Name the blood parasite species.
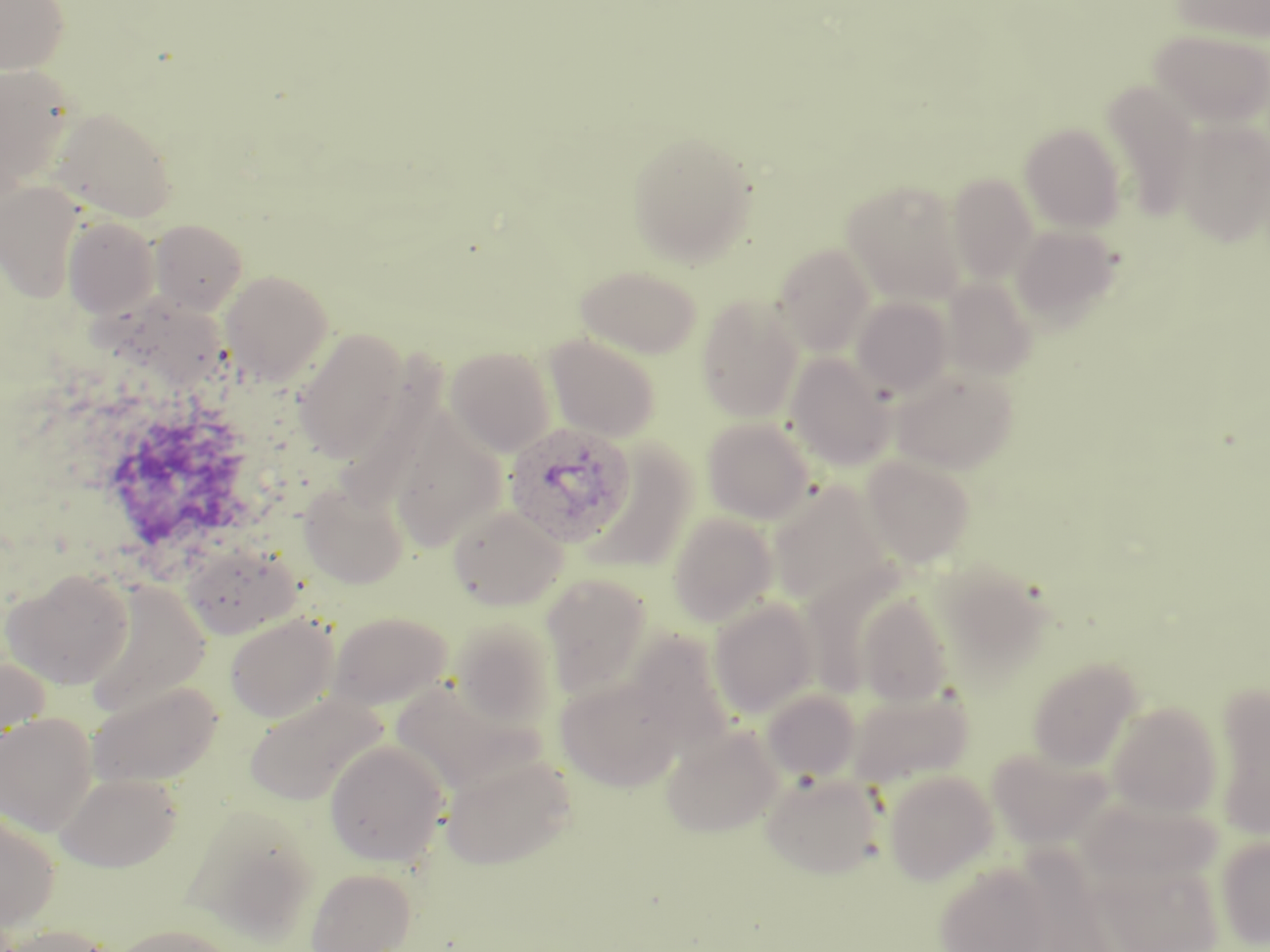

Plasmodium ovale.

Summary:
  - Coordinate format: approximate bounding boxes as named x1/y1/x2/y2 corners in pixels
  - Plasmodium ovale-infected red blood cell locations: (x1=503, y1=421, x2=636, y2=549)
  - Uninfected red blood cell locations: (x1=0, y1=0, x2=69, y2=74), (x1=1171, y1=0, x2=1270, y2=42), (x1=1150, y1=28, x2=1270, y2=128), (x1=1, y1=64, x2=77, y2=192), (x1=1101, y1=81, x2=1200, y2=219), (x1=50, y1=107, x2=178, y2=223), (x1=1174, y1=119, x2=1270, y2=247), (x1=1020, y1=123, x2=1126, y2=232), (x1=627, y1=129, x2=757, y2=267), (x1=947, y1=173, x2=1038, y2=283), (x1=842, y1=179, x2=967, y2=304), (x1=0, y1=181, x2=84, y2=302), (x1=63, y1=216, x2=160, y2=318), (x1=151, y1=219, x2=248, y2=315), (x1=1010, y1=224, x2=1123, y2=326), (x1=773, y1=244, x2=876, y2=354), (x1=576, y1=265, x2=702, y2=359), (x1=221, y1=269, x2=333, y2=384), (x1=943, y1=276, x2=1037, y2=379), (x1=91, y1=293, x2=239, y2=385), (x1=696, y1=295, x2=803, y2=422), (x1=852, y1=296, x2=953, y2=397), (x1=294, y1=329, x2=407, y2=462), (x1=545, y1=333, x2=662, y2=442), (x1=446, y1=346, x2=556, y2=456), (x1=785, y1=353, x2=896, y2=471), (x1=890, y1=369, x2=1019, y2=473), (x1=388, y1=408, x2=506, y2=553), (x1=702, y1=417, x2=815, y2=523), (x1=582, y1=442, x2=699, y2=573), (x1=861, y1=455, x2=976, y2=567), (x1=767, y1=479, x2=895, y2=611), (x1=300, y1=482, x2=408, y2=589), (x1=448, y1=504, x2=568, y2=610), (x1=668, y1=512, x2=778, y2=628), (x1=182, y1=545, x2=300, y2=639), (x1=2, y1=568, x2=135, y2=689), (x1=540, y1=573, x2=653, y2=700), (x1=83, y1=578, x2=212, y2=716), (x1=855, y1=593, x2=953, y2=706), (x1=708, y1=598, x2=818, y2=719), (x1=328, y1=611, x2=452, y2=710), (x1=225, y1=613, x2=339, y2=723), (x1=450, y1=617, x2=559, y2=727), (x1=626, y1=629, x2=739, y2=757), (x1=0, y1=653, x2=50, y2=758), (x1=1028, y1=656, x2=1143, y2=771), (x1=555, y1=676, x2=683, y2=790), (x1=85, y1=680, x2=223, y2=789), (x1=1211, y1=683, x2=1270, y2=839), (x1=845, y1=686, x2=973, y2=788), (x1=761, y1=689, x2=861, y2=782), (x1=244, y1=692, x2=387, y2=805), (x1=1106, y1=701, x2=1223, y2=818), (x1=0, y1=712, x2=98, y2=835), (x1=661, y1=723, x2=785, y2=838), (x1=324, y1=739, x2=450, y2=867), (x1=986, y1=747, x2=1113, y2=849), (x1=441, y1=752, x2=576, y2=869), (x1=761, y1=770, x2=885, y2=878), (x1=882, y1=770, x2=997, y2=885), (x1=55, y1=771, x2=183, y2=872), (x1=184, y1=803, x2=322, y2=941), (x1=0, y1=805, x2=61, y2=933), (x1=1215, y1=834, x2=1270, y2=949), (x1=1099, y1=861, x2=1224, y2=950), (x1=933, y1=862, x2=1057, y2=952), (x1=305, y1=867, x2=416, y2=952), (x1=110, y1=923, x2=241, y2=952), (x1=2, y1=924, x2=114, y2=952)
  - Modality: optical microscopy
  - Image size: 1270×952 pixels
  - Preparation: thin blood smear
  - Magnification: 1000x
  - Stain: May-Grünwald-Giemsa
  - Field of view: single